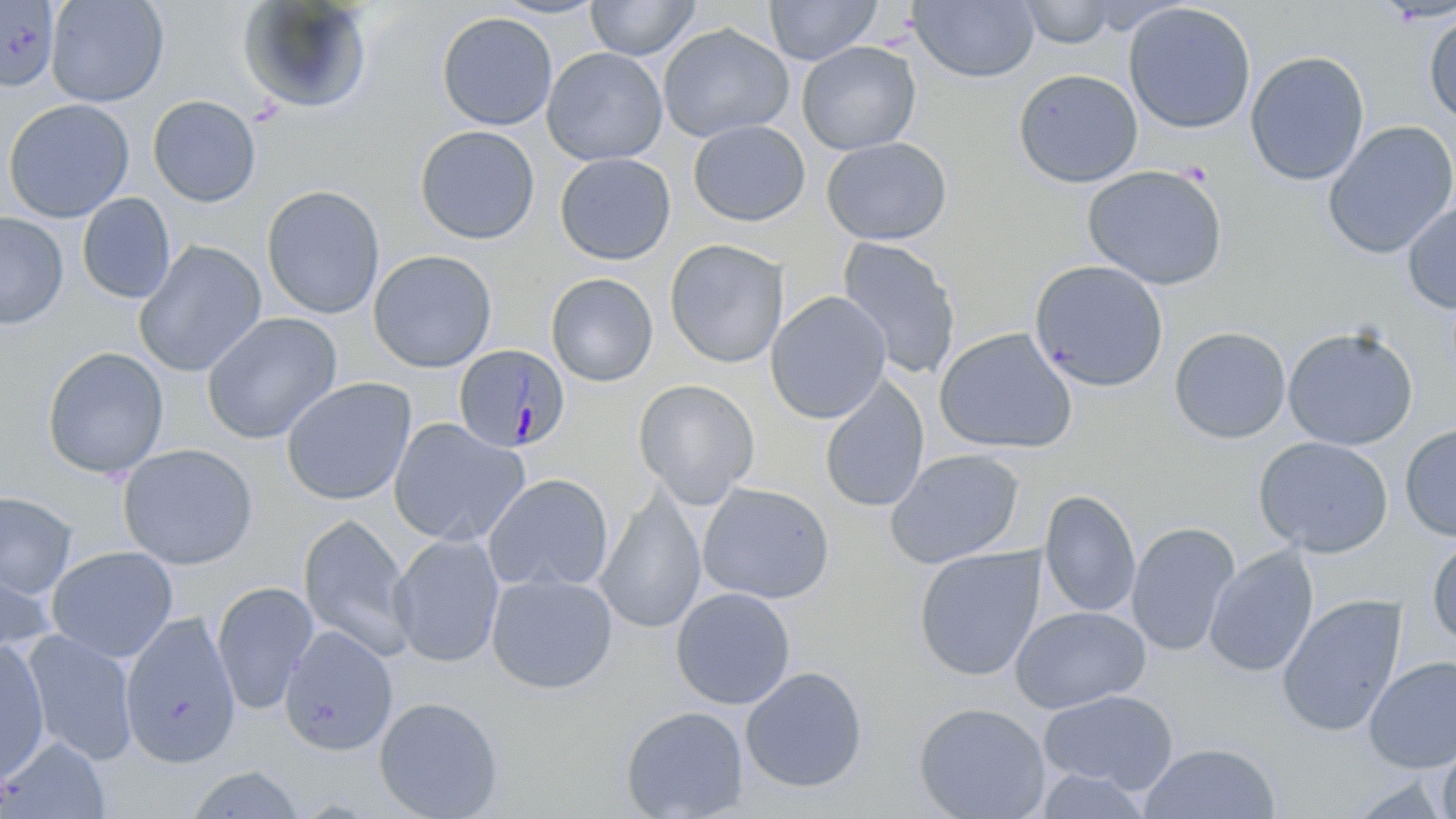
Approximate bounding boxes as (x1, y1, x2, y2) in pixels. Plasmodium malariae-infected red blood cell locations: (452, 344, 571, 453). Uninfected red blood cell locations: (45, 0, 169, 108), (585, 0, 700, 61), (765, 0, 882, 65), (1016, 0, 1120, 49), (0, 1, 61, 91), (237, 1, 374, 115), (909, 1, 1040, 84), (1122, 2, 1257, 134), (436, 11, 558, 131), (1423, 11, 1456, 126), (658, 24, 794, 143), (797, 41, 921, 155), (542, 46, 668, 165), (1245, 51, 1369, 186), (1013, 69, 1143, 188), (147, 95, 261, 207), (2, 98, 135, 223), (688, 119, 810, 226), (1322, 120, 1456, 259), (414, 125, 540, 244), (821, 137, 952, 245), (554, 152, 676, 265), (1082, 165, 1229, 290), (261, 185, 385, 319), (76, 193, 176, 304), (1401, 199, 1456, 314), (0, 212, 69, 330), (836, 236, 962, 381), (665, 238, 788, 369), (133, 239, 267, 378), (368, 250, 497, 372), (1029, 259, 1169, 392), (546, 272, 659, 387), (765, 290, 891, 424), (201, 312, 343, 444), (1282, 325, 1419, 450), (1169, 326, 1291, 444), (934, 327, 1078, 454), (42, 346, 169, 479), (819, 373, 930, 513), (280, 377, 416, 505), (633, 378, 760, 509), (388, 417, 529, 547), (1400, 423, 1456, 541), (1254, 436, 1393, 558), (117, 443, 259, 570), (884, 448, 1025, 569), (483, 473, 614, 593), (697, 481, 835, 604), (595, 486, 707, 635), (1039, 490, 1141, 619), (0, 491, 77, 599), (297, 513, 415, 659), (1125, 521, 1241, 657), (389, 533, 505, 668), (1426, 535, 1456, 650), (912, 545, 1047, 682), (1204, 545, 1319, 678), (46, 546, 178, 663), (0, 558, 58, 665), (486, 573, 618, 693), (211, 581, 318, 715), (670, 587, 796, 710), (1276, 594, 1407, 738), (1010, 605, 1151, 713), (119, 611, 241, 768), (280, 625, 398, 756), (22, 630, 139, 765), (0, 640, 51, 784), (1362, 656, 1456, 774), (740, 666, 868, 794), (1038, 688, 1179, 794), (373, 696, 505, 819), (912, 701, 1052, 819), (620, 705, 749, 819), (1, 737, 112, 818), (1436, 738, 1456, 819), (1138, 743, 1281, 819), (185, 765, 306, 819), (1032, 768, 1155, 818), (1338, 774, 1455, 818). Slide-level diagnosis: Plasmodium malariae. 1000x magnification. Thin blood film. Image is 1456×819 pixels. Light microscopy. One field of a larger specimen. May-Grünwald-Giemsa stain.